Locate every Plasmodium parasite.
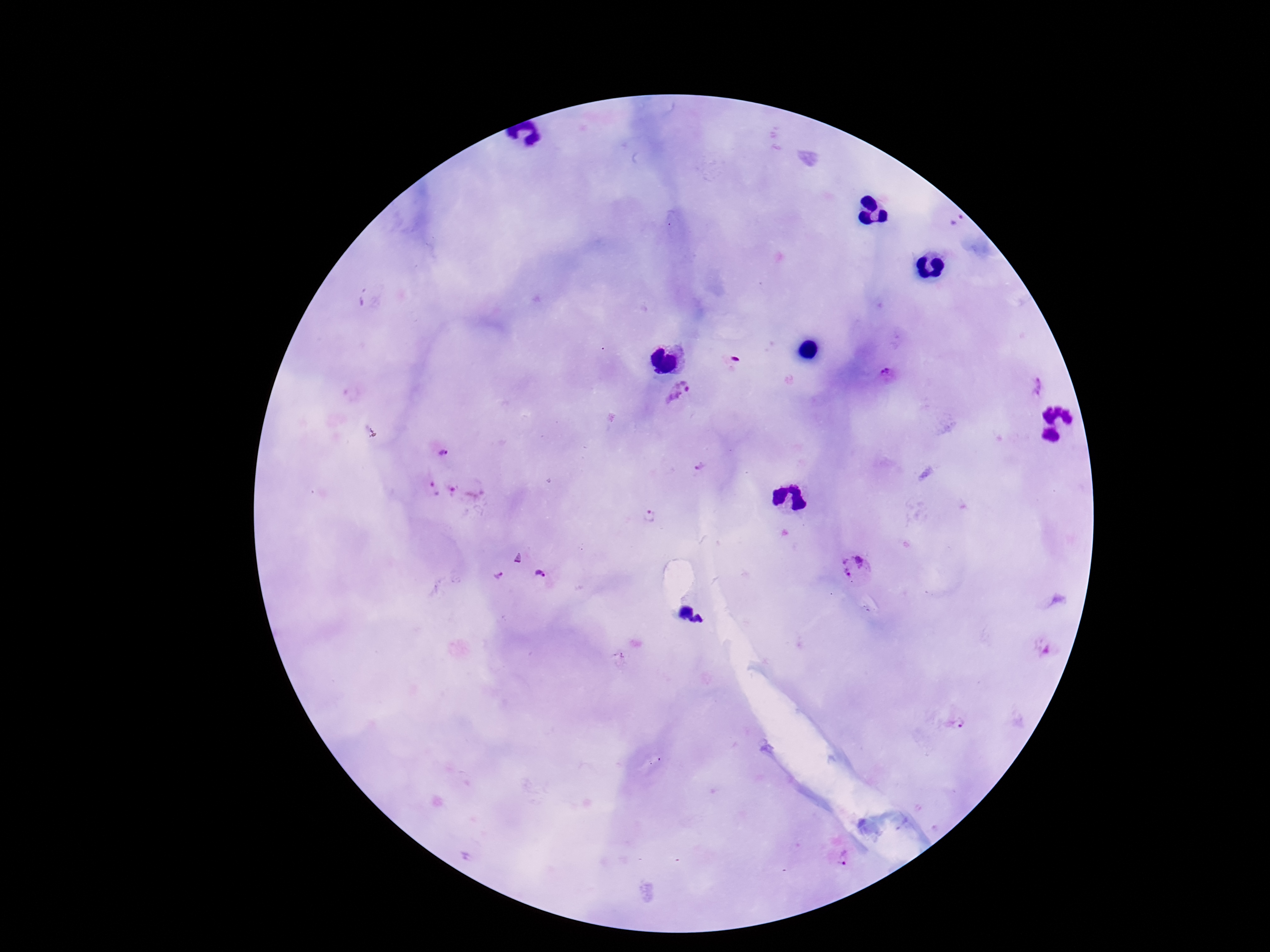
Approximate centers as (x, y) in pixels.
Plasmodium parasites: (956, 223), (734, 360), (888, 376), (1038, 387), (681, 394), (442, 455), (702, 465), (435, 490), (466, 491), (650, 517), (857, 567), (542, 575), (498, 578), (1038, 648), (956, 725), (844, 864).

Patient malaria status: infected. 100x magnification. One field from this slide. Photographed through the microscope eyepiece with a smartphone camera. Image is 1270×952 pixels. Giemsa stain. Thick blood film.